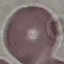
Result: negative for malaria parasites. Cell patch, automatically extracted from a larger field of view and resized to 64 × 64 pixels. Thin smear of blood. Giemsa-stained preparation. Acquired by smartphone through the microscope eyepiece.